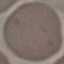
Summary:
  - Result: no malaria parasites seen
  - Stain: Giemsa
  - Capture: smartphone camera at the microscope eyepiece
  - Preparation: thin blood film
  - Image type: cell patch, automatically extracted from a larger field of view and resized to 64 × 64 pixels